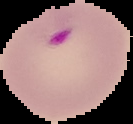
malaria status = parasitized
preparation = thin blood film
image type = cell region segmented out of the field of view; surrounding area masked to black
image size = 133×124 pixels